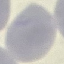

result = negative for malaria parasites
image type = cell patch, automatically extracted from a larger field of view and resized to 64 × 64 pixels
capture = smartphone camera at the microscope eyepiece
stain = Giemsa
preparation = thin blood smear